Identify the blood parasite species.
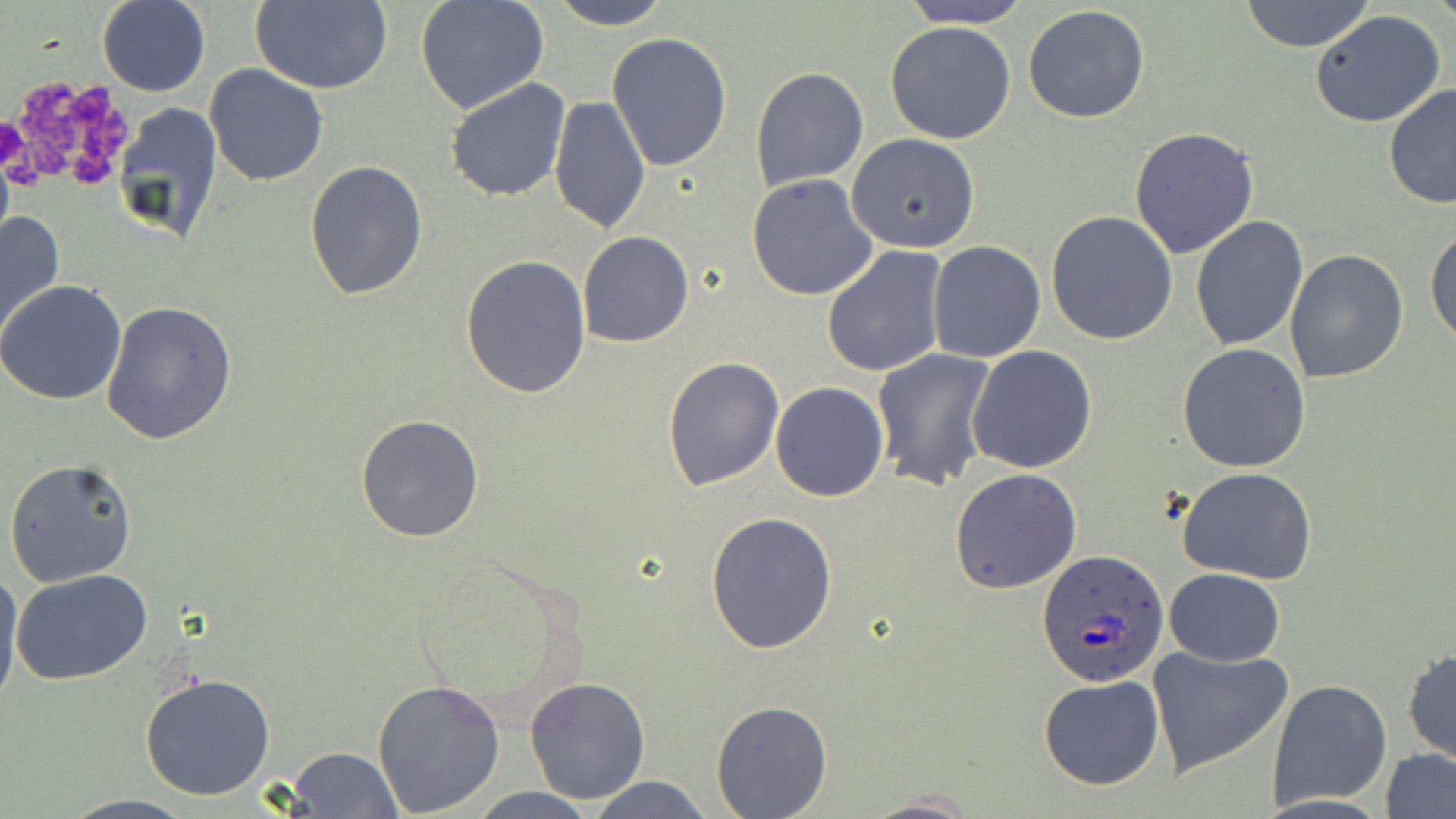
Plasmodium ovale.

Approximate bounding boxes as (x1, y1, x2, y2) in pixels. Uninfected red blood cell locations: (544, 0, 677, 28), (897, 0, 1033, 27), (1238, 0, 1376, 52), (98, 1, 211, 97), (248, 1, 393, 96), (415, 1, 549, 115), (1022, 6, 1150, 124), (1310, 10, 1448, 129), (885, 20, 1016, 143), (606, 32, 733, 175), (204, 63, 329, 186), (750, 65, 869, 193), (445, 76, 571, 202), (1384, 84, 1456, 210), (548, 94, 652, 235), (113, 102, 227, 252), (1128, 127, 1259, 258), (846, 133, 981, 254), (303, 161, 429, 300), (746, 173, 878, 302), (1047, 210, 1179, 345), (1, 211, 65, 345), (1189, 215, 1308, 352), (1426, 226, 1456, 345), (927, 229, 1172, 353), (576, 231, 694, 348), (927, 240, 1046, 362), (821, 245, 948, 378), (1283, 248, 1409, 384), (460, 254, 592, 399), (1, 280, 127, 406), (100, 299, 237, 446), (1177, 342, 1311, 471), (966, 345, 1098, 472), (872, 348, 997, 492), (661, 355, 784, 490), (770, 381, 888, 502), (355, 414, 487, 542), (5, 458, 136, 587), (949, 467, 1081, 595), (1177, 467, 1318, 585), (705, 511, 839, 655), (0, 561, 25, 714), (10, 568, 155, 684), (1164, 568, 1285, 667), (1145, 647, 1293, 775), (1403, 649, 1456, 763), (138, 673, 276, 801), (1038, 675, 1165, 790), (372, 677, 505, 816), (522, 677, 650, 805), (1266, 679, 1394, 812), (712, 700, 832, 816), (286, 747, 403, 818), (1382, 748, 1456, 819), (584, 775, 713, 818), (464, 787, 604, 819), (861, 793, 977, 819), (59, 795, 200, 818). Plasmodium ovale-infected red blood cell locations: (1038, 550, 1170, 688). Platelet locations: (70, 88, 115, 127), (26, 136, 66, 178), (68, 146, 112, 184). May-Grünwald-Giemsa stain. Image is 1456×819 pixels. 1000x magnification. Optical microscopy. Thin blood film. Single field of view.